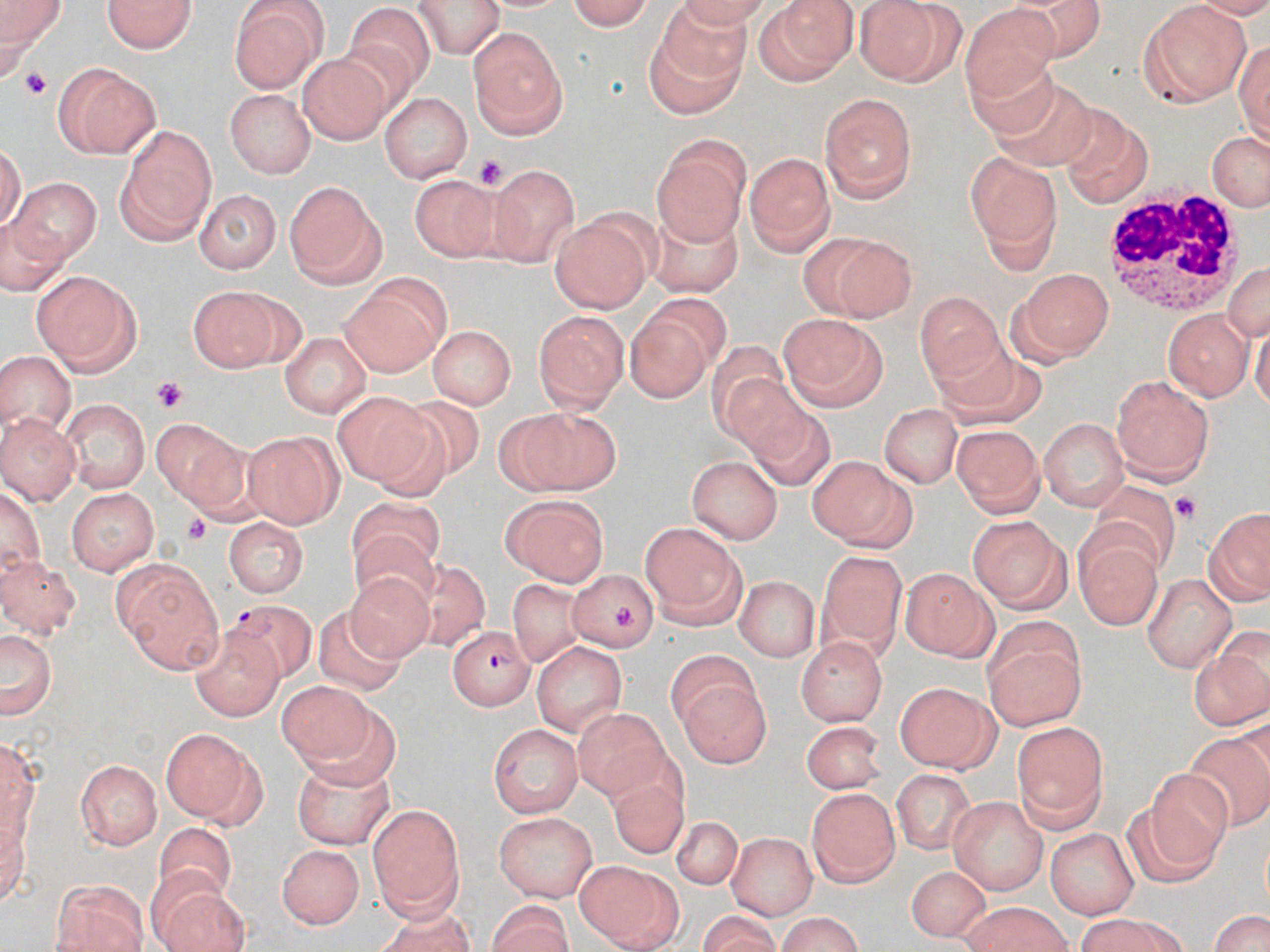
slide_level_diagnosis: Plasmodium falciparum
image_size: 1270×952 pixels
preparation: thin blood smear
platelet_locations: 'approximate bounding boxes as (x1,y1)-(x2,y2) corner pairs in pixels: (472,155)-(505,185), (149,377)-(187,412), (1172,491)-(1198,524), (181,514)-(218,548), (612,604)-(639,631)'
magnification: 1000x
modality: optical microscopy
stain: May-Grünwald-Giemsa
field_of_view: single
plasmodium_falciparum_infected_red_blood_cell_locations: 'approximate bounding boxes as (x1,y1)-(x2,y2) corner pairs in pixels: (228,602)-(314,681), (451,624)-(532,707)'
white_blood_cell_locations: 'approximate bounding boxes as (x1,y1)-(x2,y2) corner pairs in pixels: (1106,190)-(1240,316)'
uninfected_red_blood_cell_locations: 'approximate bounding boxes as (x1,y1)-(x2,y2) corner pairs in pixels: (108,0)-(192,58), (559,0)-(653,29), (2,1)-(65,55), (414,1)-(504,56), (669,1)-(774,26), (856,1)-(963,85), (230,2)-(328,94), (755,2)-(857,86), (1140,2)-(1251,103), (349,3)-(437,86), (962,4)-(1059,98), (657,5)-(755,84), (469,25)-(569,138), (644,33)-(743,118), (1235,36)-(1270,143), (962,51)-(1059,141), (295,53)-(395,145), (53,61)-(161,158), (996,86)-(1094,165), (228,87)-(315,178), (383,93)-(469,183), (823,93)-(916,200), (1067,121)-(1152,209), (116,123)-(219,241), (1205,129)-(1270,213), (652,134)-(752,243), (746,153)-(836,255), (963,154)-(1060,266), (489,164)-(579,263), (415,173)-(496,267), (10,177)-(99,265), (280,178)-(383,286), (197,190)-(279,271), (645,211)-(746,298), (552,217)-(652,313), (799,232)-(915,322), (1225,260)-(1270,346), (1013,267)-(1113,361), (32,270)-(142,374), (338,275)-(447,376), (191,286)-(276,374), (915,290)-(1003,383), (648,292)-(730,370), (1162,308)-(1252,400), (533,310)-(627,416), (777,314)-(889,412), (625,315)-(708,403), (426,326)-(516,410), (280,333)-(371,420), (0,353)-(77,437), (938,358)-(1053,424), (721,365)-(815,461), (1111,375)-(1213,482), (330,392)-(436,485), (392,394)-(490,487), (63,395)-(149,494), (880,397)-(963,487), (753,408)-(838,489), (0,413)-(80,502), (505,414)-(624,497), (1038,415)-(1131,510), (151,418)-(249,511), (955,426)-(1045,516), (242,430)-(341,526), (807,453)-(916,551), (689,454)-(787,544), (1095,483)-(1176,572), (68,485)-(160,575), (347,494)-(449,570), (498,494)-(610,586), (1203,508)-(1270,606), (966,514)-(1072,612), (225,518)-(309,599), (640,520)-(747,625), (348,527)-(444,606), (1076,535)-(1160,629), (819,551)-(906,646), (0,554)-(78,635), (110,555)-(226,676), (405,561)-(488,645), (901,567)-(997,661), (342,568)-(437,665), (568,569)-(658,651), (1142,571)-(1236,671), (736,575)-(820,661), (510,579)-(589,670), (319,604)-(403,699), (983,622)-(1090,731), (190,625)-(285,722), (0,626)-(57,723), (1189,632)-(1268,731), (796,636)-(889,727), (532,639)-(626,738), (670,657)-(771,772), (895,678)-(1003,771), (280,681)-(381,767), (570,711)-(670,797), (489,721)-(581,814), (799,721)-(892,794), (1013,724)-(1105,830), (159,727)-(262,823), (1186,731)-(1270,828), (74,758)-(162,850), (291,758)-(391,849), (892,766)-(980,853), (1144,770)-(1235,867), (611,781)-(695,853), (808,787)-(898,888), (947,793)-(1046,892), (1119,803)-(1221,887), (366,804)-(467,923), (494,812)-(598,902), (669,812)-(739,886), (151,819)-(242,894), (1041,824)-(1138,917), (725,832)-(815,917), (276,841)-(366,931), (575,859)-(681,952), (902,864)-(994,941), (50,877)-(149,952), (157,884)-(258,952), (482,899)-(574,950), (377,903)-(473,952), (956,903)-(1073,952), (1205,903)-(1270,952), (772,914)-(867,950), (1070,916)-(1198,952)'